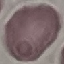 Malaria status: uninfected. Cell patch, automatically extracted from a larger field of view and resized to 64 × 64 pixels. Acquired by smartphone through the microscope eyepiece. Giemsa-stained preparation. Thin smear of blood.